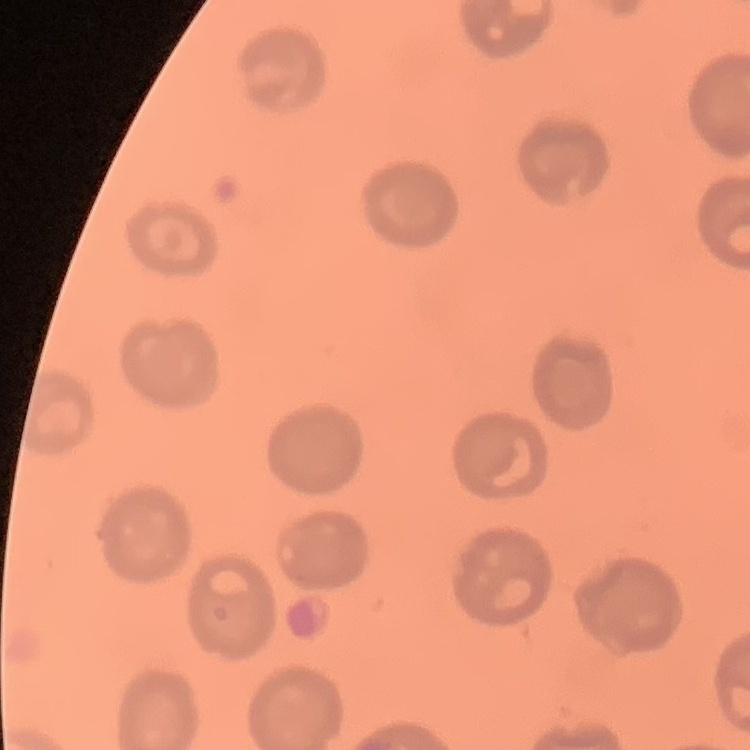

The red blood cells exhibit no rouleaux formation. Thin peripheral smear. One tile cut from a larger photomicrograph. Field's or Giemsa stain.